Describe the morphology of the erythrocytes.
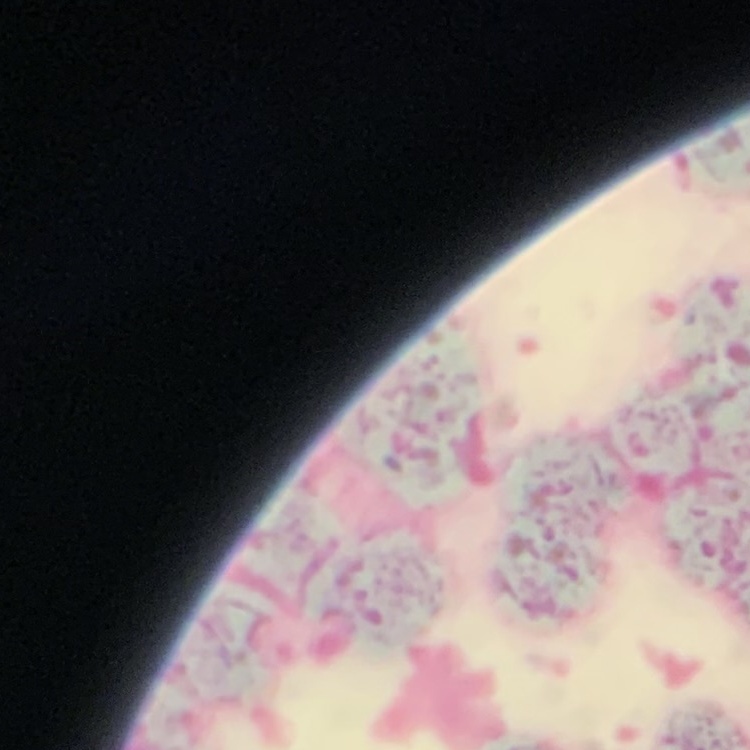
Rouleaux formation.

Summary:
  - Preparation: thin blood smear
  - Image type: square crop of a larger photomicrograph
  - Stain: Field's or Giemsa